Evaluate for malaria.
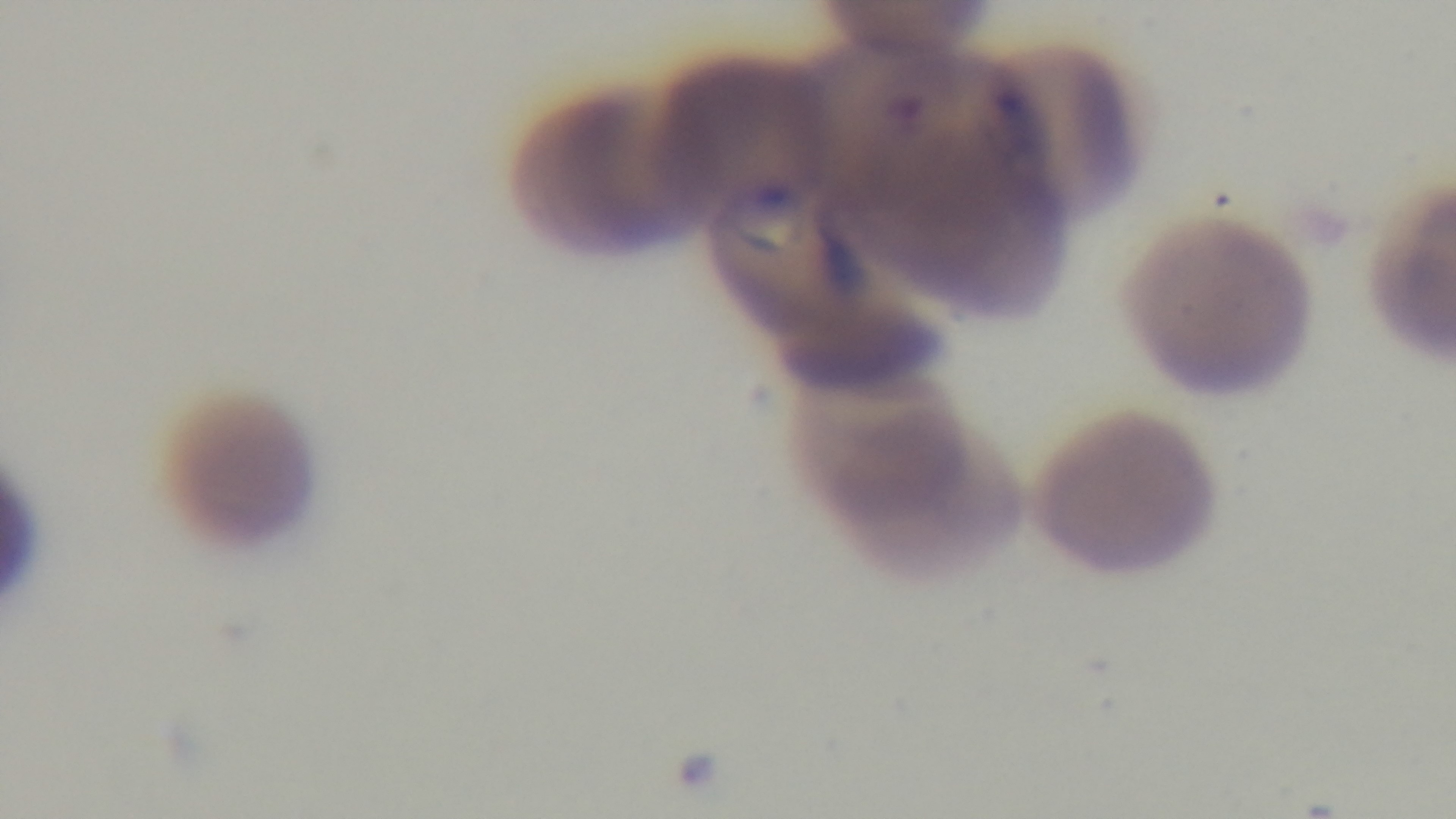

Positive.

stain: Giemsa
modality: light microscopy
field_of_view: one from the slide
preparation: thin smear
objective: 100x oil immersion
capture: mounted 4K digital camera